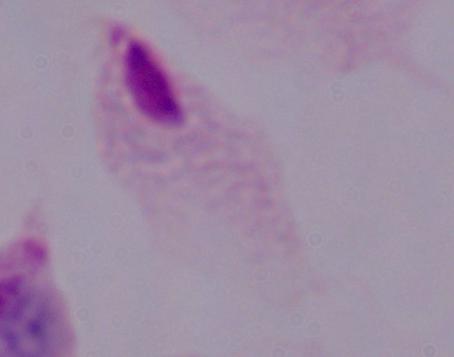

1000x magnification. Micrograph. A trichomonad is shown.